Report the malaria status of this cell.
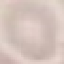
Uninfected.

image_type: cell patch, automatically extracted from a larger field of view and resized to 64 × 64 pixels
capture: smartphone through the microscope eyepiece
preparation: thin smear
stain: Giemsa